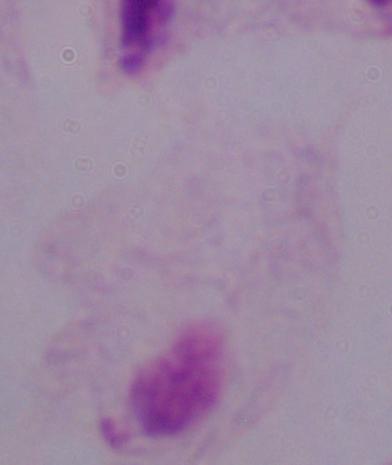

Summary:
  - Identification: trichomonad
  - Magnification: 1000x
  - Modality: photomicrograph